Outline each blood parasite and name the species.
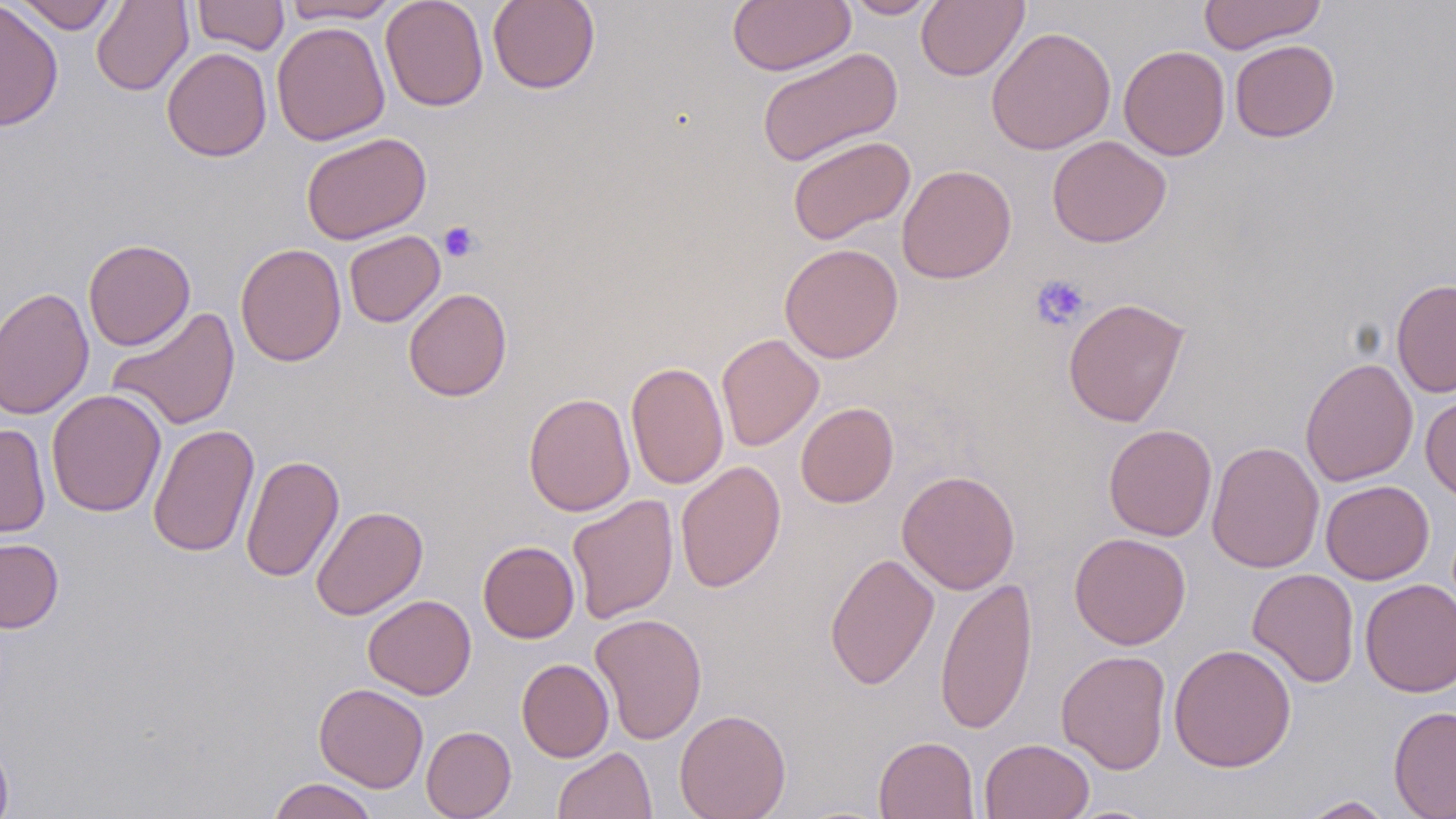
No blood parasites seen.

Summary:
  - Coordinate format: approximate bounding boxes as (x1, y1, x2, y2) in pixels
  - Platelet locations: (438, 221, 481, 263), (1030, 274, 1090, 330)
  - Uninfected red blood cell locations: (11, 0, 122, 34), (192, 0, 289, 55), (380, 0, 489, 111), (487, 0, 601, 94), (727, 0, 855, 75), (842, 0, 944, 19), (917, 0, 1028, 81), (1197, 0, 1327, 54), (0, 1, 63, 131), (92, 1, 193, 95), (281, 1, 401, 23), (271, 21, 390, 146), (986, 26, 1116, 155), (1229, 39, 1340, 142), (1118, 44, 1230, 160), (755, 46, 903, 168), (161, 47, 272, 162), (300, 131, 432, 245), (787, 135, 916, 245), (1047, 135, 1172, 247), (897, 164, 1017, 284), (344, 230, 445, 328), (83, 238, 195, 351), (235, 243, 346, 367), (779, 243, 903, 363), (1391, 278, 1456, 397), (1, 285, 95, 420), (403, 287, 512, 401), (1063, 297, 1190, 427), (107, 306, 240, 431), (716, 333, 824, 451), (1300, 357, 1418, 487), (625, 360, 729, 490), (46, 389, 166, 517), (523, 392, 636, 516), (1420, 392, 1456, 502), (796, 402, 898, 507), (0, 423, 51, 538), (148, 424, 260, 558), (1103, 424, 1218, 542), (1207, 441, 1324, 574), (240, 454, 345, 583), (675, 461, 787, 592), (896, 470, 1021, 595), (1321, 479, 1434, 585), (567, 493, 679, 624), (311, 505, 428, 621), (1069, 532, 1191, 650), (0, 538, 64, 633), (478, 540, 579, 643), (825, 552, 940, 690), (1247, 568, 1360, 688), (934, 576, 1038, 734), (1360, 579, 1456, 698), (363, 594, 476, 699), (590, 613, 707, 744), (1169, 643, 1296, 772), (1056, 650, 1171, 774), (517, 658, 613, 762), (314, 683, 428, 792), (1388, 705, 1456, 819), (674, 708, 791, 819), (421, 725, 517, 819), (873, 736, 980, 819), (0, 737, 13, 819), (979, 738, 1094, 818), (552, 746, 657, 819), (268, 778, 379, 819), (1296, 795, 1397, 818)
  - Slide-level diagnosis: no evidence of blood parasites
  - Field of view: one of a larger specimen
  - Magnification: 1000x
  - Preparation: thin blood film
  - Modality: optical microscopy
  - Stain: May-Grünwald-Giemsa
  - Image size: 1456×819 pixels